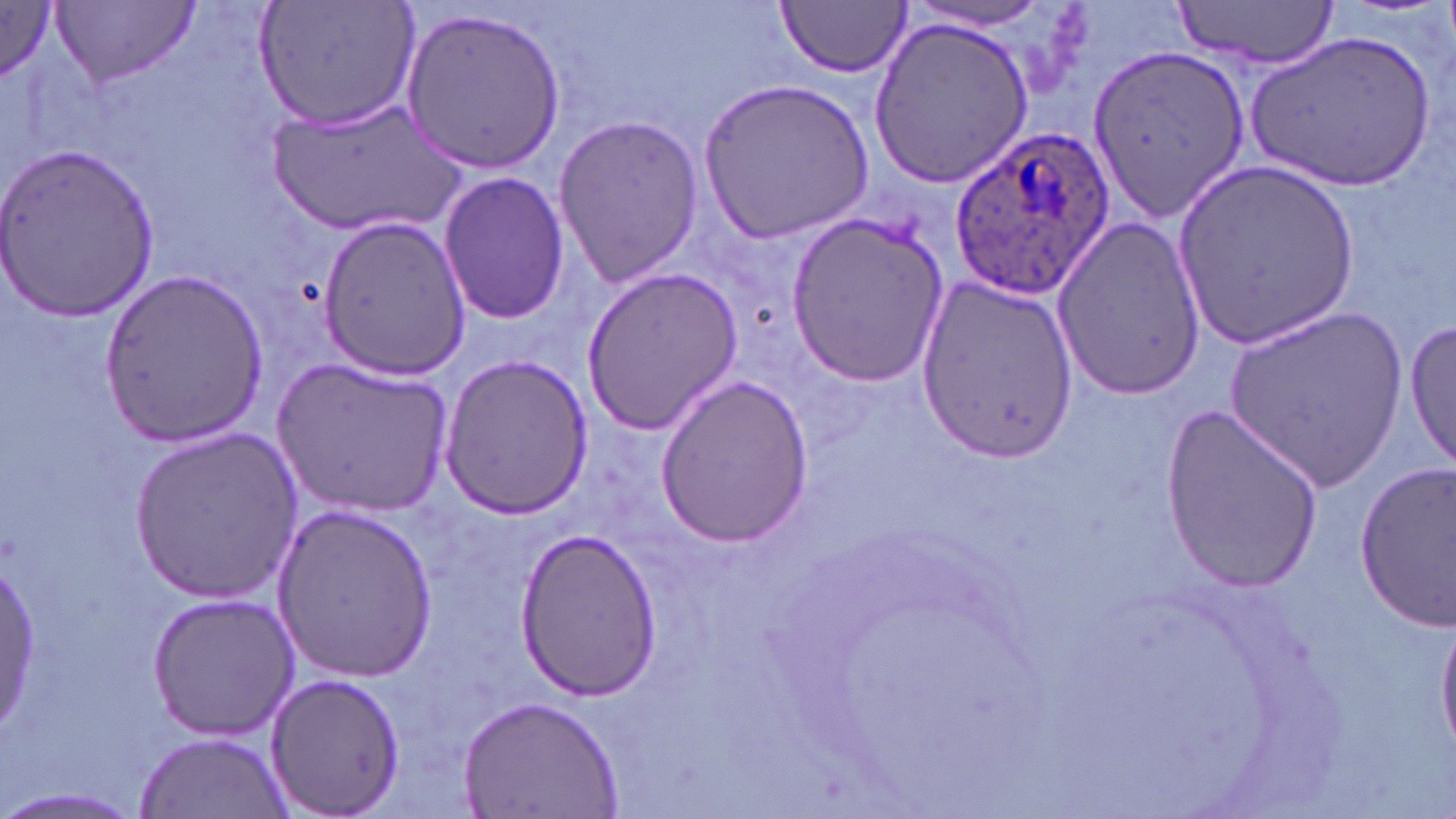
Summary:
  - Coordinate format: approximate bounding boxes as (x1, y1, x2, y2) in pixels
  - Plasmodium ovale-infected red blood cell locations: (950, 133, 1112, 301)
  - Uninfected red blood cell locations: (253, 0, 424, 134), (1168, 0, 1344, 68), (0, 1, 67, 83), (776, 1, 912, 77), (56, 2, 197, 88), (901, 2, 1057, 33), (400, 8, 565, 173), (869, 16, 1035, 188), (1248, 31, 1435, 195), (1088, 40, 1250, 223), (699, 76, 873, 242), (269, 98, 462, 238), (552, 113, 704, 288), (0, 143, 159, 322), (1172, 160, 1359, 351), (438, 170, 570, 327), (785, 211, 949, 390), (1050, 211, 1207, 405), (315, 214, 471, 378), (579, 266, 744, 435), (100, 268, 268, 450), (914, 274, 1079, 458), (1222, 307, 1411, 489), (1404, 315, 1454, 471), (438, 352, 594, 519), (273, 358, 452, 520), (653, 375, 814, 546), (1159, 404, 1325, 589), (129, 424, 303, 601), (1354, 459, 1456, 633), (270, 505, 439, 682), (515, 530, 663, 699), (0, 557, 43, 725), (148, 591, 300, 740), (1437, 615, 1456, 758), (265, 671, 406, 815), (457, 694, 626, 819), (133, 731, 296, 818), (0, 788, 148, 816)
  - Slide-level diagnosis: Plasmodium ovale
  - Magnification: 1000x
  - Modality: light microscopy
  - Preparation: thin blood film
  - Stain: May-Grünwald-Giemsa
  - Image size: 1456×819 pixels
  - Field of view: one of a larger specimen